Assess for malaria.
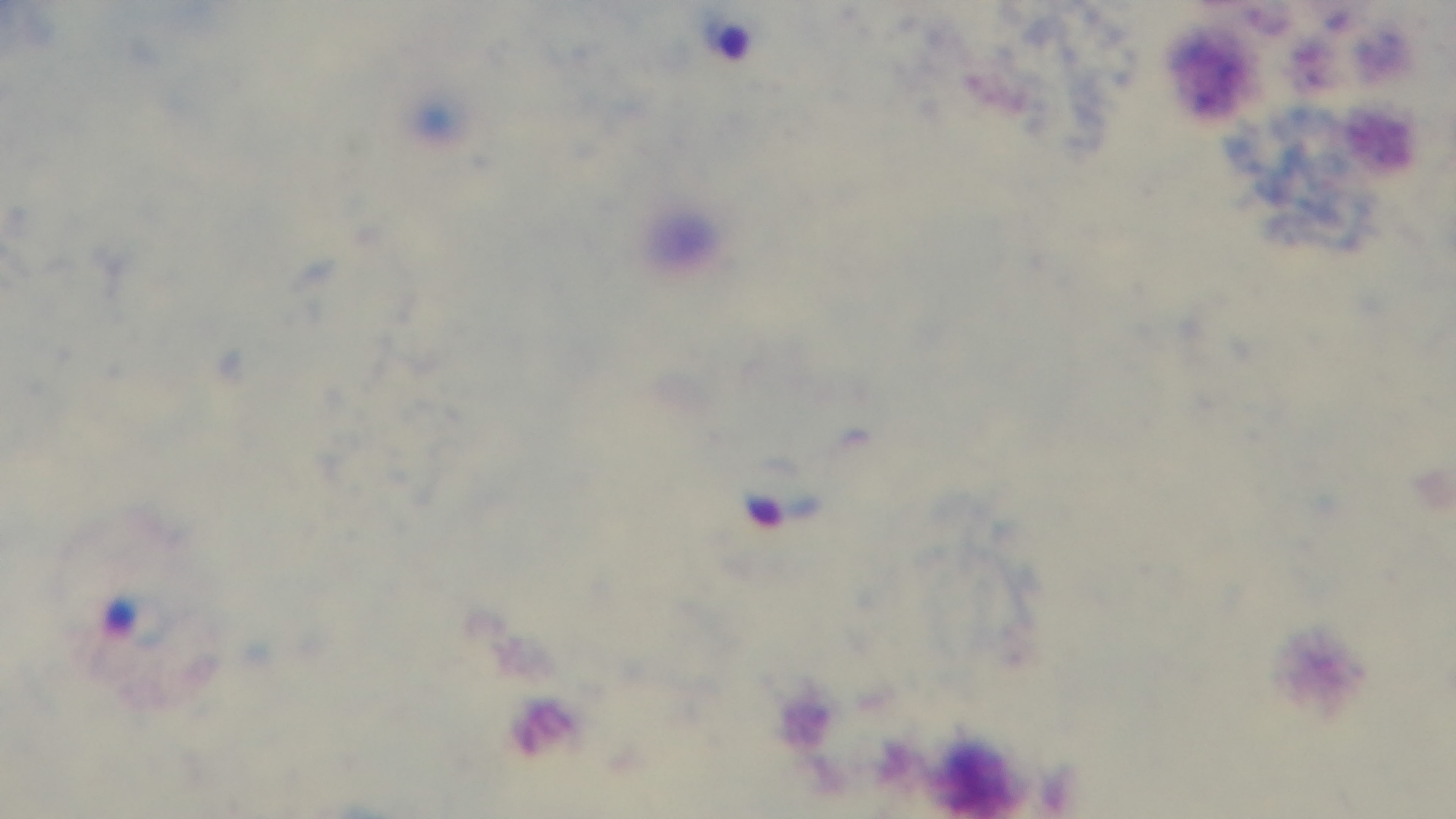

Infected.

field of view = single
modality = light microscopy
preparation = thick blood film
stain = Giemsa
objective = 100x oil immersion
capture = mounted 4K digital camera